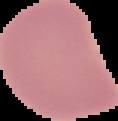
Malaria status: uninfected. From a thin blood smear. Cell region segmented out of the field of view; the surrounding area is masked to black. Image is 118×121 pixels.